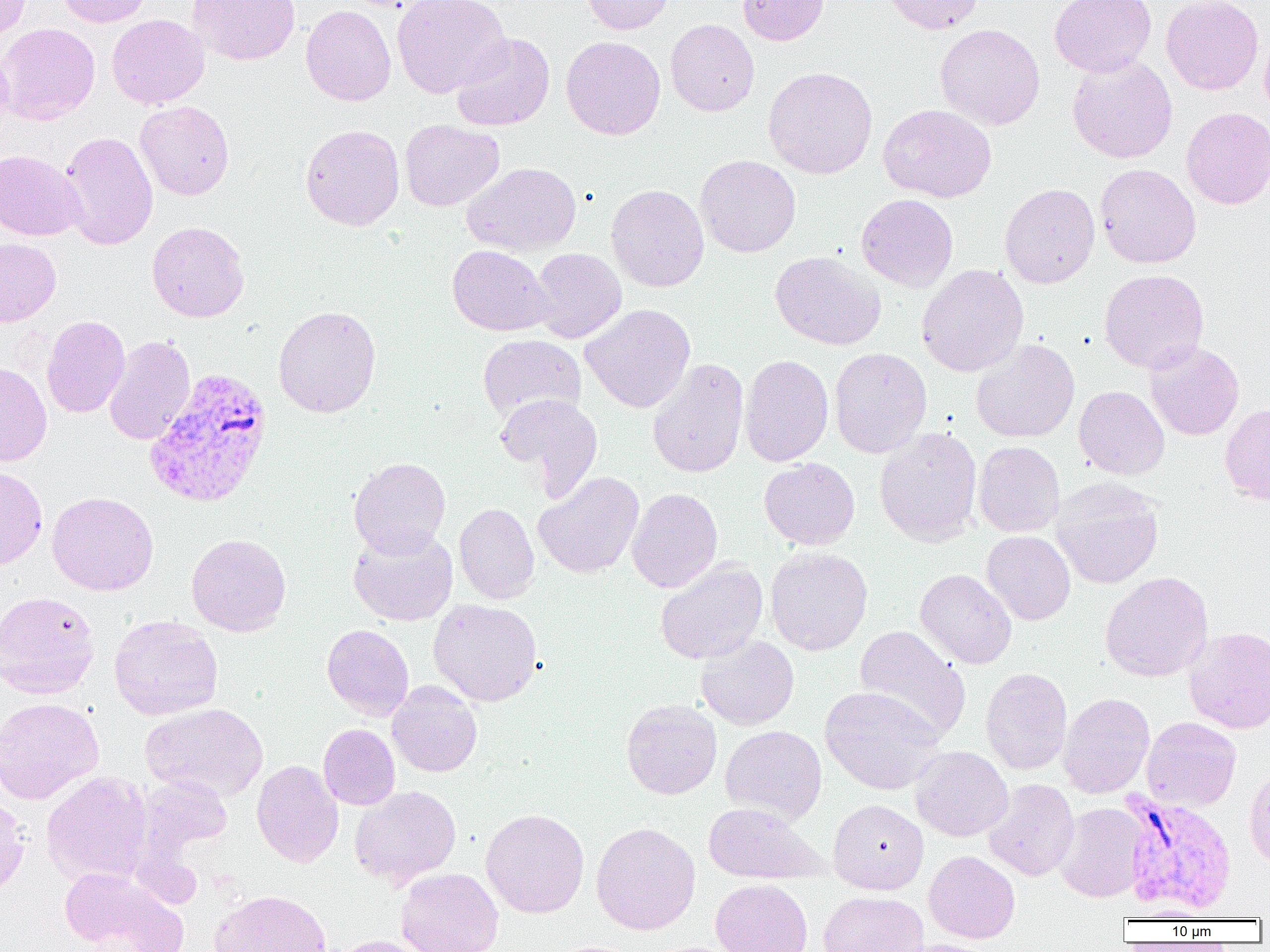

Summary:
  - Coordinate format: approximate bounding boxes as (x1, y1, x2, y2) in pixels
  - Plasmodium vivax-infected red blood cell locations: (144, 366, 274, 508), (1119, 791, 1236, 915)
  - Uninfected red blood cell locations: (0, 0, 32, 41), (56, 0, 153, 27), (188, 0, 300, 65), (392, 0, 511, 98), (580, 0, 674, 34), (737, 0, 829, 46), (880, 0, 984, 34), (1049, 0, 1156, 78), (1161, 0, 1264, 95), (301, 4, 396, 105), (107, 14, 209, 108), (665, 19, 759, 116), (0, 23, 100, 125), (935, 24, 1045, 130), (1259, 26, 1270, 124), (451, 33, 554, 131), (561, 36, 665, 140), (0, 43, 13, 137), (1067, 54, 1177, 164), (763, 67, 878, 179), (135, 100, 235, 200), (878, 104, 996, 202), (1181, 107, 1270, 209), (400, 120, 504, 211), (300, 124, 405, 231), (59, 131, 158, 251), (0, 150, 84, 241), (695, 155, 801, 257), (463, 162, 581, 256), (1095, 163, 1201, 268), (1000, 183, 1099, 288), (606, 184, 709, 292), (856, 194, 959, 292), (147, 222, 249, 322), (0, 238, 61, 326), (447, 244, 555, 336), (529, 248, 626, 343), (770, 251, 886, 350), (916, 264, 1028, 377), (1099, 269, 1209, 374), (580, 304, 695, 413), (273, 305, 381, 418), (42, 315, 130, 418), (477, 334, 586, 423), (103, 335, 196, 446), (971, 338, 1079, 443), (1145, 341, 1244, 440), (829, 346, 932, 458), (739, 354, 834, 467), (647, 358, 748, 478), (0, 362, 52, 466), (1074, 386, 1169, 479), (496, 393, 603, 499), (1220, 403, 1270, 506), (874, 426, 982, 547), (973, 441, 1065, 537), (349, 457, 451, 557), (759, 457, 860, 550), (0, 467, 47, 571), (533, 471, 645, 579), (1051, 481, 1164, 589), (626, 487, 723, 592), (47, 491, 158, 595), (454, 503, 539, 604), (348, 526, 458, 626), (981, 530, 1076, 625), (186, 533, 291, 637), (765, 546, 872, 655), (654, 559, 768, 665), (915, 568, 1017, 669), (1100, 571, 1214, 682), (0, 591, 100, 698), (428, 598, 543, 706), (109, 615, 223, 720), (322, 624, 414, 720), (854, 625, 971, 742), (1184, 626, 1270, 734), (696, 635, 799, 730), (981, 667, 1072, 775), (387, 681, 483, 777), (820, 685, 944, 795), (1058, 693, 1155, 798), (0, 697, 103, 805), (621, 699, 722, 799), (141, 703, 268, 801), (1142, 716, 1242, 811), (318, 723, 400, 810), (720, 724, 827, 823), (910, 746, 1013, 841), (251, 759, 343, 868), (1243, 765, 1270, 870), (41, 771, 154, 887), (136, 775, 234, 856), (983, 779, 1079, 881), (350, 785, 461, 888), (0, 792, 30, 900), (828, 799, 929, 892), (703, 802, 828, 884), (1055, 802, 1148, 902), (480, 808, 589, 918), (591, 821, 701, 935), (923, 850, 1021, 944), (59, 867, 186, 951), (396, 867, 504, 952), (710, 879, 812, 952), (209, 889, 331, 952), (818, 891, 928, 952), (331, 935, 434, 952)
  - Slide-level diagnosis: Plasmodium vivax
  - Preparation: thin blood film
  - Field of view: single
  - Image size: 1270×952 pixels
  - Modality: optical microscopy
  - Magnification: 1000x